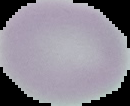

Summary:
  - Preparation: thin blood smear
  - Image size: 130×106 pixels
  - Image type: cell region segmented out of the field of view; surrounding area masked to black
  - Malaria status: uninfected